Classify this cell by malaria status.
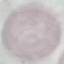

Uninfected.

Summary:
  - Capture: smartphone through the microscope eyepiece
  - Image type: cell patch, automatically extracted from a larger field of view and resized to 64 × 64 pixels
  - Preparation: thin blood smear
  - Stain: Giemsa